Draw a bounding box around every parasitised red blood cell.
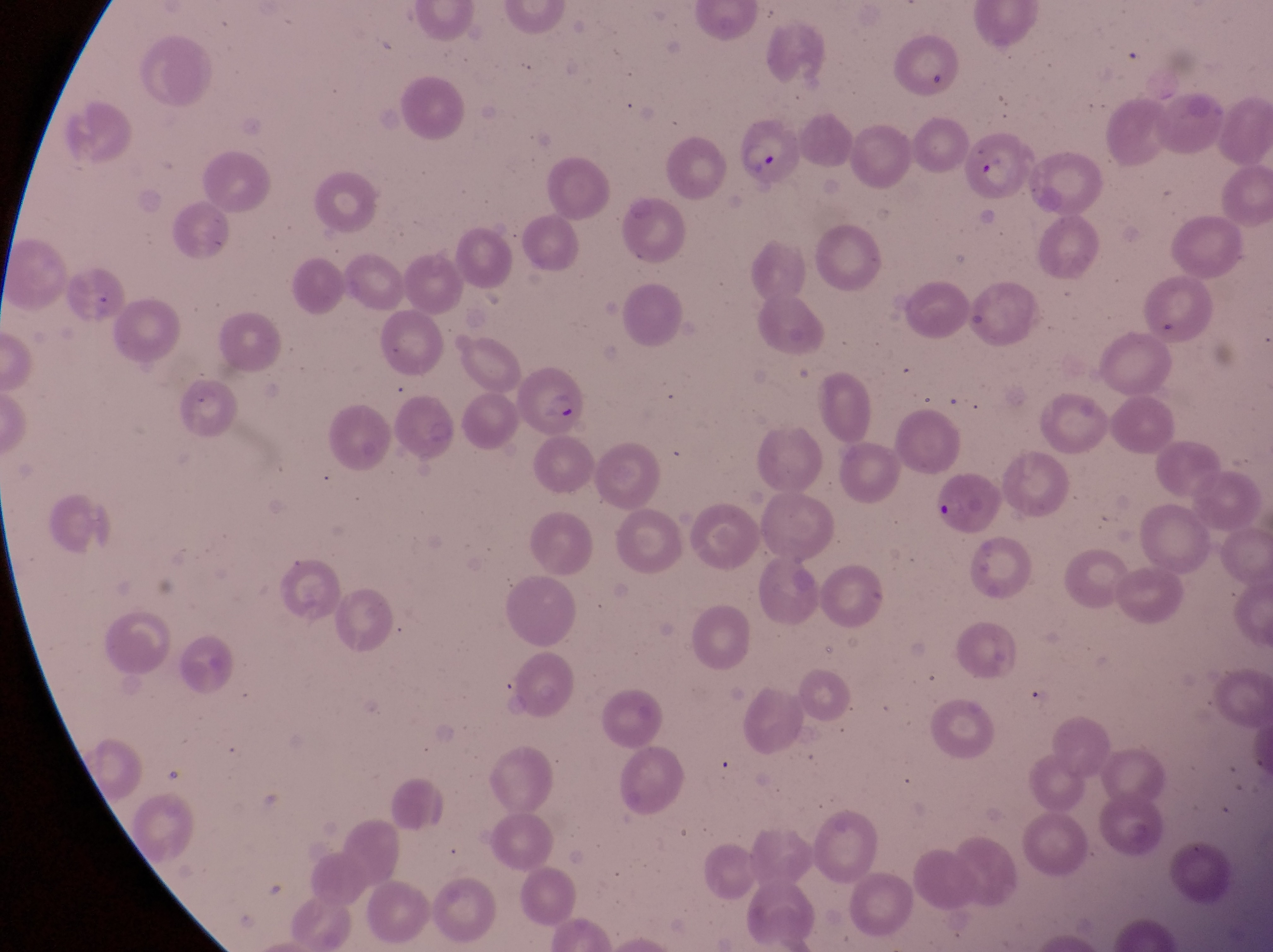

Approximate bounding boxes as {left, top, right, bottom} in pixels.
Parasitised red blood cells: {898, 40, 965, 97}, {731, 120, 808, 192}, {964, 137, 1033, 202}, {514, 369, 589, 443}, {931, 477, 1000, 535}.

Summary:
  - Preparation: thin blood film
  - Capture: smartphone photograph through the eyepiece of an Olympus CX-23 microscope
  - Country: Uganda
  - Image size: 1273×952 pixels
  - Magnification: 1000x
  - Field of view: single